Give the position of every leukocyte visible.
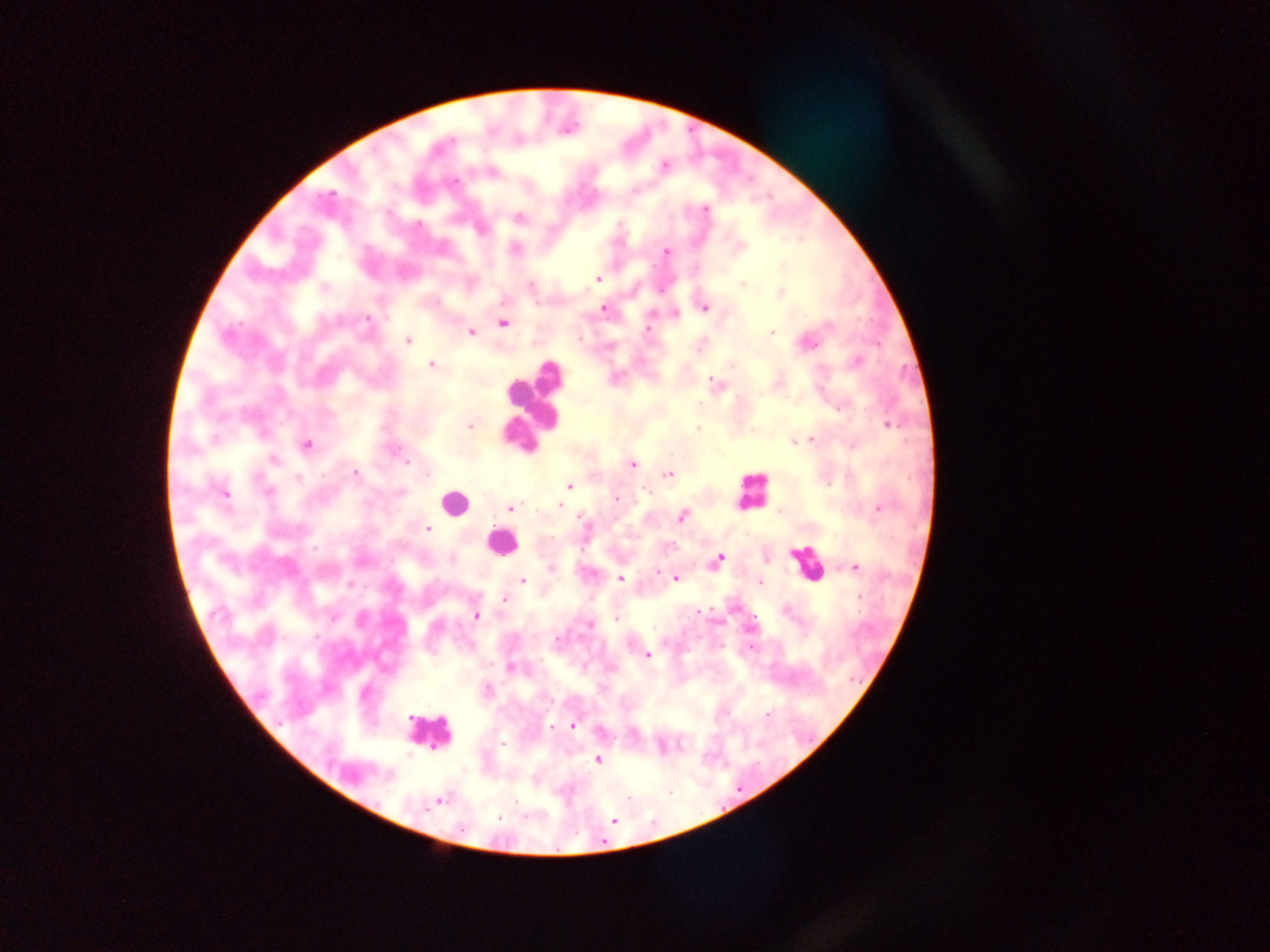
Approximate centers as (x, y) in pixels.
Leukocytes: (535, 402), (750, 491), (456, 502), (501, 543), (808, 563), (428, 732).

capture = mobile-phone photograph through a microscope
preparation = thick blood film
image size = 1270×952 pixels
field of view = single
Plasmodium parasite locations = approximate centers as (x, y) in pixels: (664, 165), (455, 182), (329, 195), (705, 209), (519, 218), (419, 224), (666, 252), (597, 279), (531, 285), (743, 285), (781, 293), (604, 309), (704, 309), (368, 318), (504, 324), (648, 329), (471, 332), (771, 333), (407, 341), (810, 344), (857, 361), (431, 365), (733, 365), (711, 380), (887, 425), (470, 426), (698, 429), (811, 439), (794, 442), (307, 444), (396, 450), (275, 460), (407, 461), (632, 463), (356, 474), (427, 474), (668, 474), (298, 478), (569, 485), (268, 491), (224, 493), (400, 493), (616, 499), (559, 506), (878, 508), (511, 509), (682, 517), (583, 521), (427, 529), (719, 558), (855, 568), (657, 572), (676, 578), (621, 579), (523, 580), (760, 582), (859, 597), (504, 599), (698, 611), (476, 615), (617, 618), (556, 639), (647, 655), (510, 668), (488, 690), (768, 714), (573, 725), (552, 726), (502, 744), (598, 759), (389, 775), (439, 801), (498, 817), (614, 821)
country = Ghana